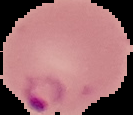
Summary:
  - Image type: cell region segmented out of the field of view; surrounding area masked to black
  - Image size: 133×115 pixels
  - Malaria status: parasitized
  - Preparation: thin blood film